Report the malaria status of this cell.
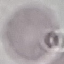

It is uninfected.

Summary:
  - Image type: cell patch, automatically extracted from a larger field of view and resized to 64 × 64 pixels
  - Capture: smartphone through the microscope eyepiece
  - Preparation: thin blood smear
  - Stain: Giemsa